Assess this cell for malaria.
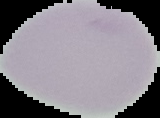

Uninfected.

{
  "image_size": "160×118 pixels",
  "image_type": "cell region segmented out of the field of view; surrounding area masked to black",
  "preparation": "thin blood film"
}